Locate every white blood cell.
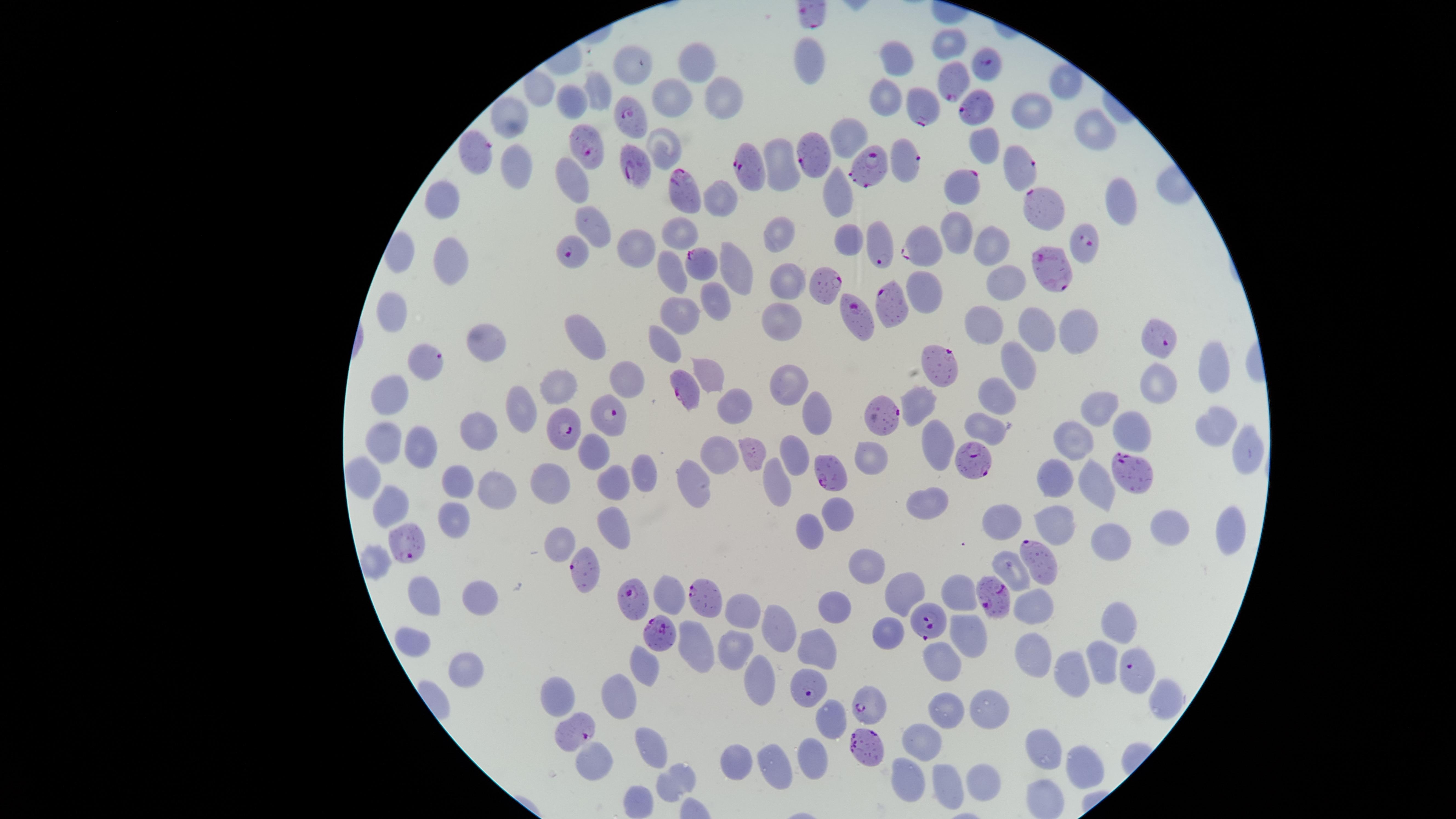
No white blood cells identified.

{
  "capture": "smartphone photograph through the microscope eyepiece",
  "preparation": "thin smear of blood",
  "uninfected_red_blood_cells": "approximate marker points, in pixels from the top-left corner: (x=947, y=41), (x=695, y=59), (x=812, y=59), (x=894, y=60), (x=1070, y=79), (x=723, y=89), (x=535, y=91), (x=596, y=91), (x=674, y=95), (x=885, y=95), (x=571, y=105), (x=1027, y=107), (x=509, y=118), (x=1098, y=128), (x=845, y=131), (x=663, y=137), (x=984, y=145), (x=514, y=162), (x=782, y=164), (x=573, y=173), (x=834, y=191), (x=441, y=195), (x=720, y=198), (x=1118, y=201), (x=590, y=217), (x=956, y=227), (x=677, y=230), (x=780, y=234), (x=848, y=237), (x=987, y=241), (x=633, y=245), (x=402, y=253), (x=451, y=253), (x=737, y=262), (x=669, y=271), (x=788, y=280), (x=1004, y=280), (x=714, y=294), (x=391, y=312), (x=680, y=315), (x=781, y=315), (x=984, y=323), (x=1034, y=325), (x=1074, y=328), (x=578, y=334), (x=480, y=337), (x=662, y=341), (x=1018, y=364), (x=1210, y=365), (x=709, y=368), (x=627, y=375), (x=1159, y=381), (x=787, y=382), (x=563, y=385), (x=996, y=392), (x=387, y=394), (x=916, y=398), (x=739, y=402), (x=1099, y=404), (x=517, y=405), (x=816, y=405), (x=1214, y=416), (x=1126, y=426), (x=984, y=427), (x=479, y=428), (x=1073, y=437), (x=387, y=440), (x=420, y=440), (x=933, y=442), (x=596, y=448), (x=722, y=452), (x=1240, y=452), (x=753, y=454), (x=794, y=455), (x=868, y=463), (x=645, y=472), (x=550, y=473), (x=358, y=474), (x=1057, y=480), (x=458, y=482), (x=610, y=482), (x=778, y=483), (x=692, y=484), (x=1097, y=490), (x=491, y=491), (x=928, y=503), (x=389, y=507), (x=845, y=512), (x=453, y=521), (x=1006, y=522), (x=1056, y=523), (x=609, y=525), (x=1165, y=525), (x=1229, y=526), (x=813, y=530), (x=1115, y=544), (x=562, y=546), (x=869, y=564), (x=1015, y=565), (x=902, y=587), (x=957, y=591), (x=424, y=592), (x=667, y=593), (x=1034, y=600), (x=482, y=601), (x=835, y=609), (x=740, y=613), (x=1113, y=618), (x=970, y=628), (x=890, y=631), (x=783, y=636), (x=415, y=642), (x=697, y=648), (x=730, y=648), (x=816, y=648), (x=1035, y=650), (x=937, y=661), (x=1101, y=661), (x=467, y=663), (x=645, y=670), (x=758, y=675), (x=1073, y=684), (x=623, y=693), (x=562, y=696), (x=1168, y=697), (x=990, y=707), (x=832, y=711), (x=946, y=714), (x=651, y=740), (x=920, y=747), (x=1043, y=754), (x=814, y=757), (x=589, y=761), (x=735, y=762), (x=1082, y=764), (x=775, y=769), (x=979, y=777), (x=904, y=779), (x=677, y=780), (x=945, y=785), (x=1048, y=800), (x=640, y=801)",
  "field_of_view": "single",
  "presence": "malaria parasites identified",
  "parasitized_red_blood_cells": "approximate marker points, in pixels from the top-left corner: (x=989, y=63), (x=952, y=79), (x=920, y=105), (x=978, y=107), (x=632, y=117), (x=584, y=143), (x=478, y=151), (x=816, y=153), (x=907, y=160), (x=1020, y=165), (x=746, y=170), (x=869, y=170), (x=638, y=173), (x=956, y=183), (x=684, y=193), (x=1041, y=210), (x=1080, y=240), (x=924, y=241), (x=880, y=244), (x=575, y=249), (x=700, y=263), (x=1049, y=272), (x=826, y=286), (x=891, y=302), (x=856, y=315), (x=1156, y=337), (x=426, y=359), (x=938, y=364), (x=686, y=389), (x=614, y=416), (x=884, y=416), (x=565, y=429), (x=970, y=455), (x=1128, y=467), (x=407, y=540), (x=1035, y=557), (x=583, y=573), (x=998, y=596), (x=700, y=597), (x=634, y=601), (x=929, y=622), (x=660, y=636), (x=1140, y=674), (x=806, y=687), (x=864, y=704), (x=573, y=731), (x=860, y=748)",
  "stain": "Giemsa",
  "species": "Plasmodium falciparum",
  "image_size": "1456×819 pixels",
  "visible_region": "circular"
}